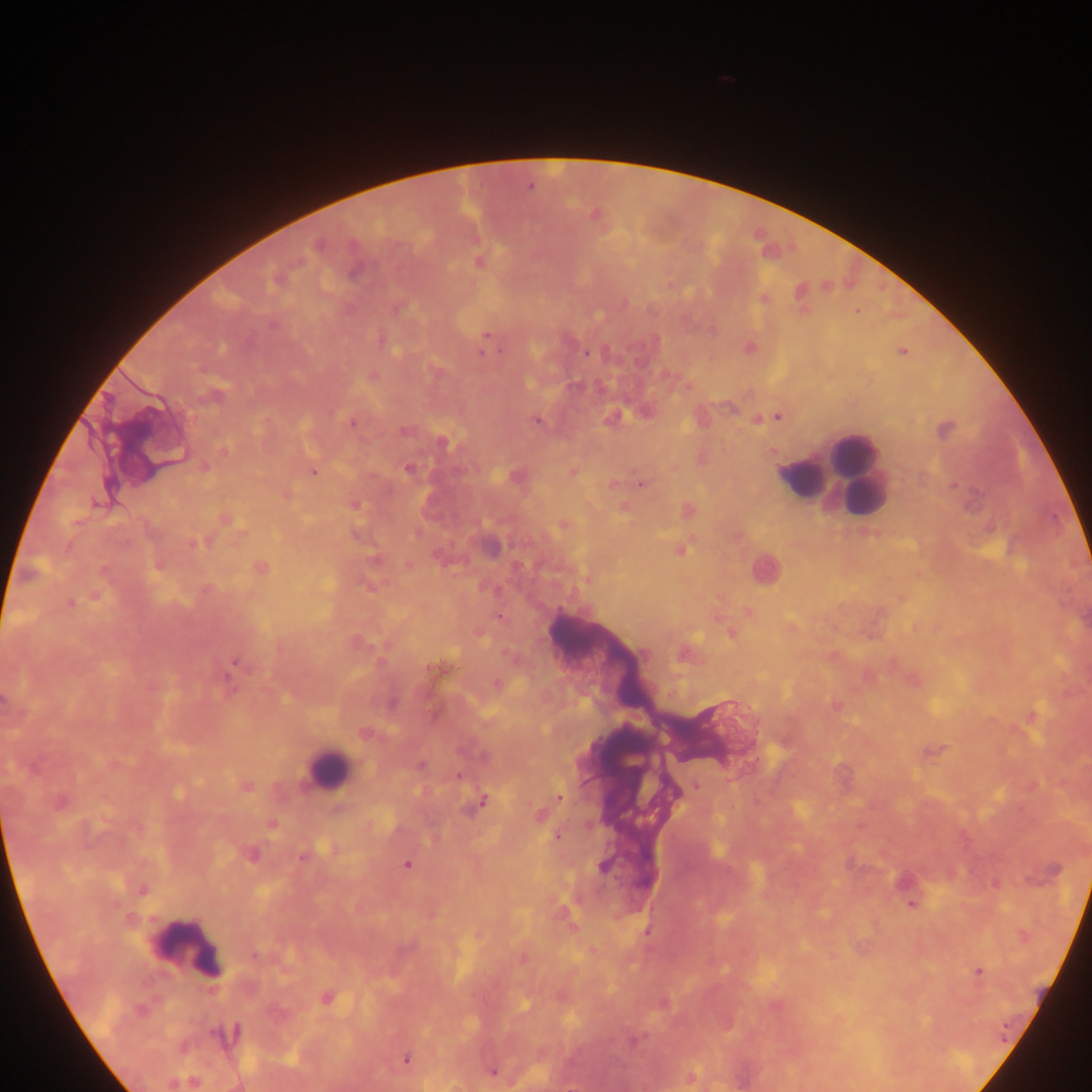
Approximate centers as x y in pixels. Plasmodium parasite locations: 530 187; 595 215; 318 245; 479 263; 354 272; 858 311; 487 335; 483 353; 586 354; 373 376; 216 396; 613 417; 778 417; 537 421; 352 424; 403 431; 442 442; 223 450; 206 467; 408 470; 312 472; 641 484; 356 505; 624 507; 225 519; 563 525; 196 543; 680 551; 261 567; 588 580; 70 603; 498 616; 731 633; 643 653; 234 662; 496 683; 836 706; 421 765; 459 776; 248 786; 696 786; 559 797; 483 801; 59 802; 540 815; 273 825; 557 837; 251 855; 302 859; 407 865; 603 867; 142 890; 911 905; 647 932; 254 956; 979 971; 326 998; 139 1010; 225 1035; 405 1059; 492 1072; 692 1078. Leukocyte locations: 852 452; 828 473; 803 477; 486 543; 764 569; 328 769; 188 945. One field of view. Photographed through a microscope with a mobile-phone camera. Collected in Ghana. Image is 1092×1092 pixels. Thick blood smear.